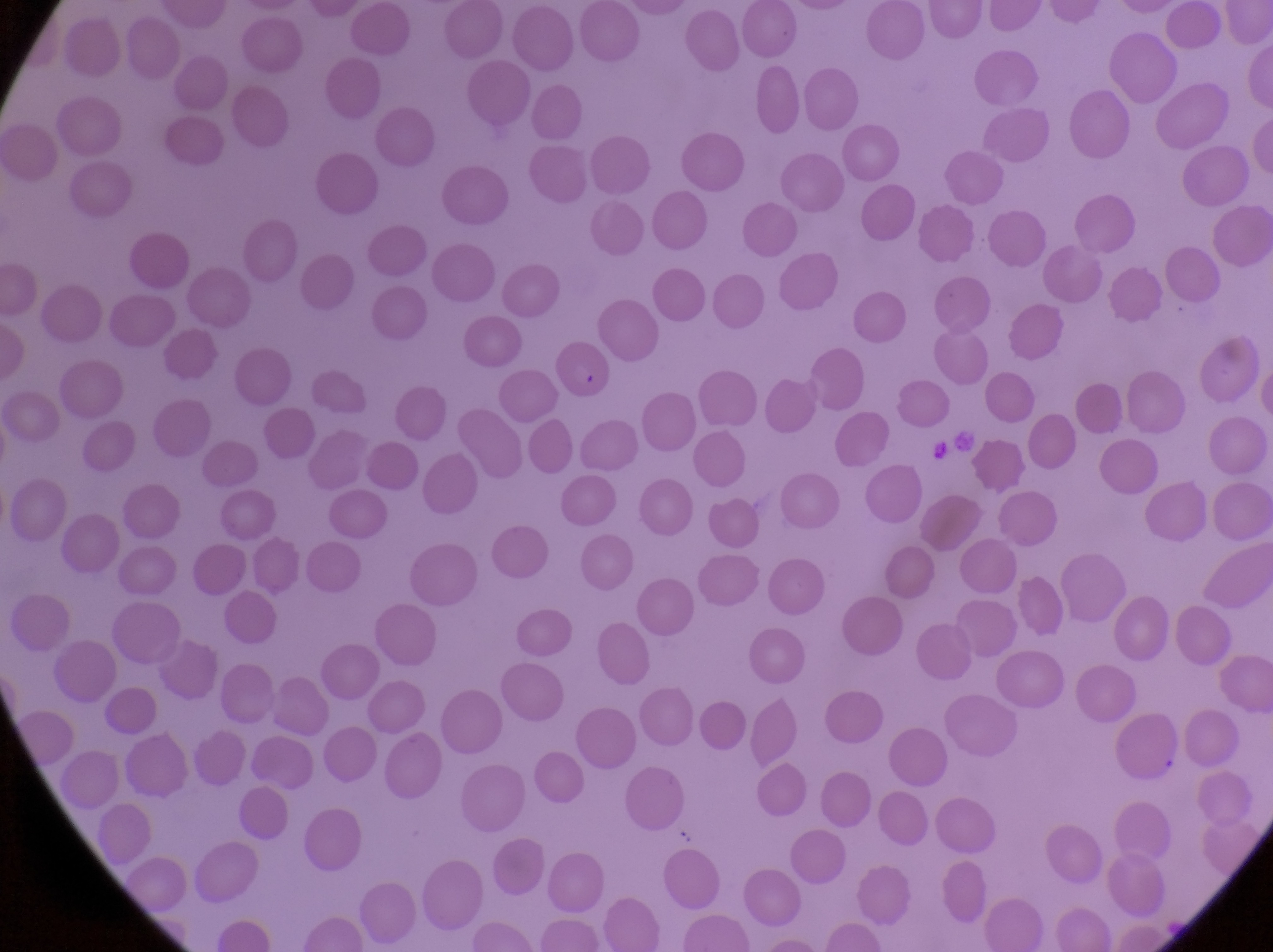

Approximate bounding boxes as left top right bottom in pixels. Artifact (platelet-like body, stain precipitate, or debris) locations: 926 441 953 461. Parasitised red blood cell locations: 551 339 616 404. Thin blood film. Captured by a smartphone held over the eyepiece of an Olympus CX-23 microscope. At a magnification of 1000x. Collected in Uganda. One field of view. Image is 1273×952 pixels.